Comment on the morphology of the red blood cells.
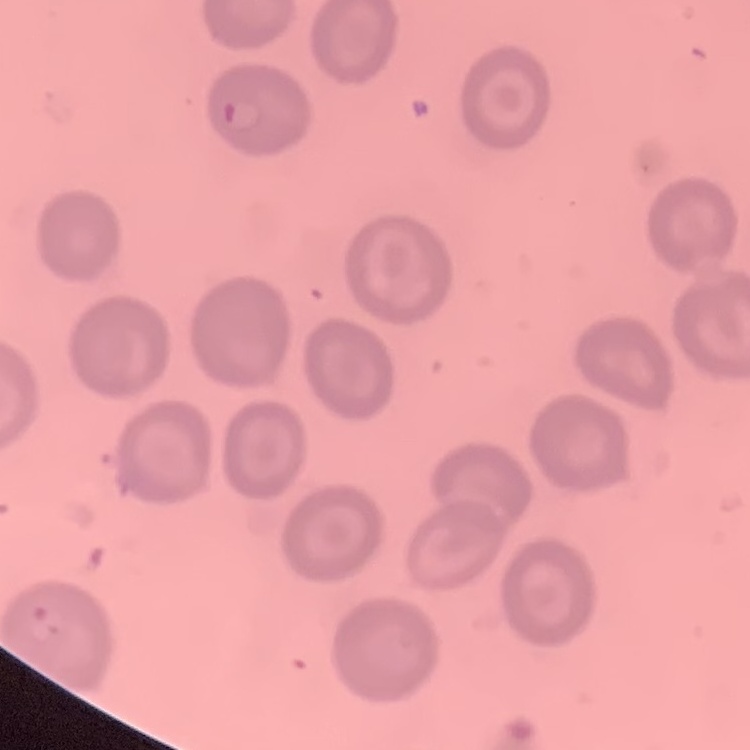

They show no rouleaux formation.

stain = Field's or Giemsa
preparation = thin peripheral smear
image type = one tile cut from a larger photomicrograph